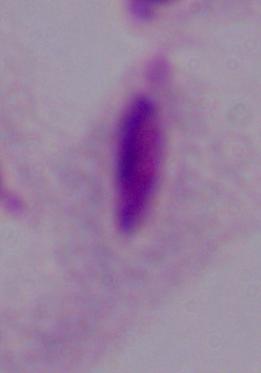
{
  "identification": "trichomonad",
  "magnification": "1000x",
  "modality": "photomicrograph"
}